Classify this cell by malaria status.
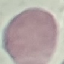

Uninfected.

capture = smartphone through the microscope eyepiece
preparation = thin blood film
image type = cell patch, automatically extracted from a larger field of view and resized to 64 × 64 pixels
stain = Giemsa